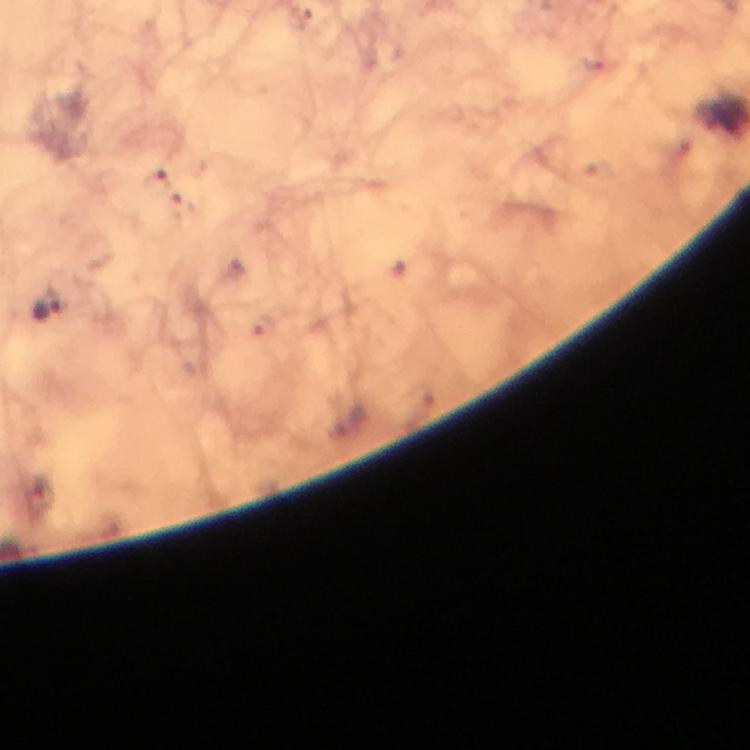

Approximate centers as (x, y) in pixels. Malaria parasite locations: (48, 308). Image is 750×750 pixels. Cropped region of a single field of view. Thick blood film. Giemsa-stained preparation. From a diagnostic examination for malaria. 100x magnification. Photographed with a smartphone mounted on the microscope. Immersion oil applied.